State the blood parasite species.
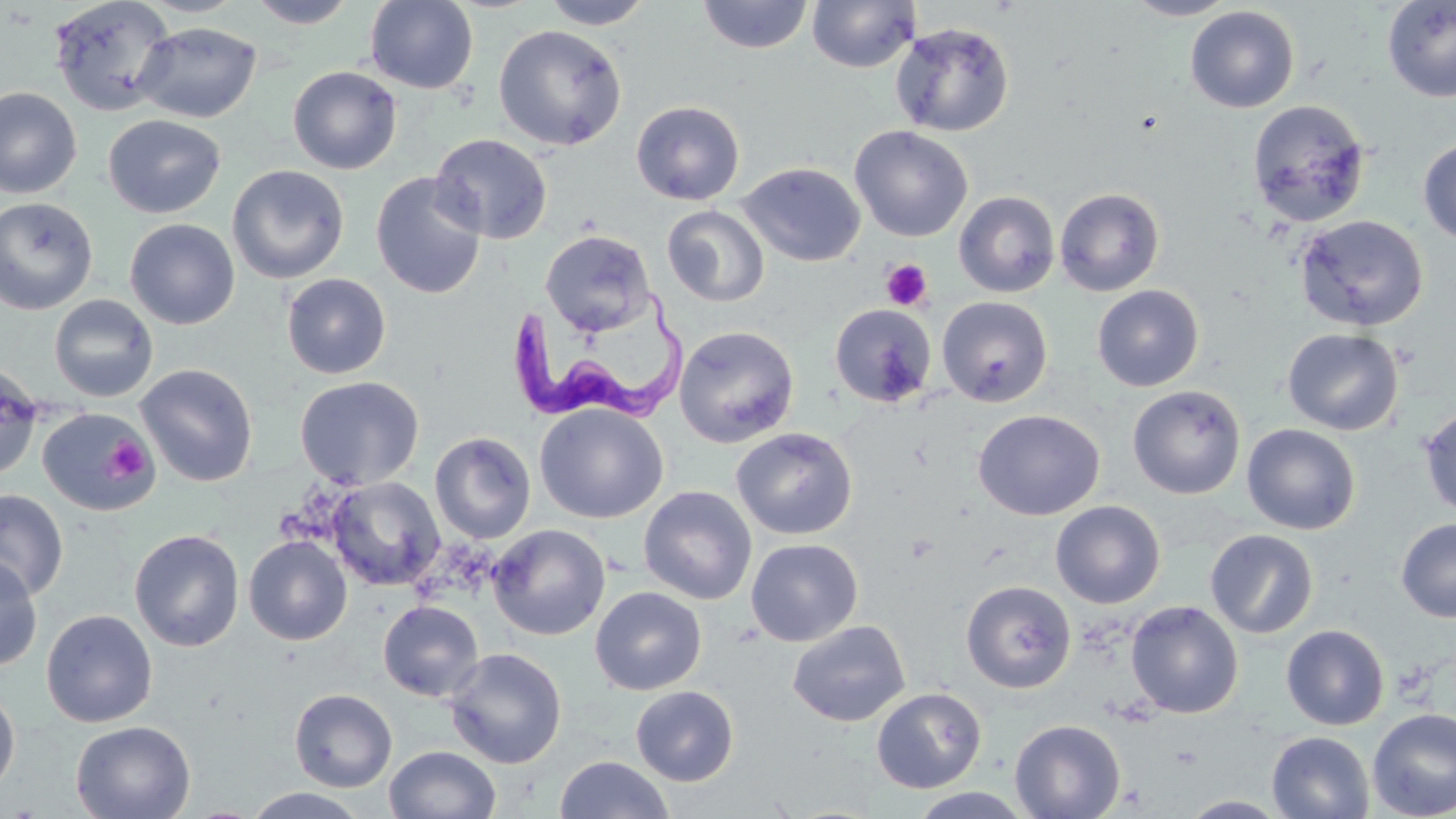
Trypanosoma brucei.

Summary:
  - Coordinate format: approximate bounding boxes as (x1, y1, x2, y2) in pixels
  - Platelet locations: (881, 259, 933, 311), (104, 437, 152, 482)
  - Trypanosoma brucei locations: (505, 288, 690, 426)
  - Uninfected red blood cell locations: (49, 0, 176, 117), (139, 0, 246, 17), (245, 0, 359, 29), (365, 0, 479, 94), (541, 0, 655, 29), (697, 0, 814, 54), (806, 0, 920, 73), (1123, 0, 1240, 20), (1382, 1, 1456, 103), (1185, 6, 1300, 113), (134, 21, 262, 123), (890, 22, 1015, 137), (493, 24, 628, 151), (287, 66, 402, 174), (0, 87, 82, 199), (1247, 99, 1371, 227), (631, 100, 745, 205), (102, 114, 226, 219), (849, 125, 973, 242), (430, 133, 552, 244), (1418, 138, 1456, 245), (737, 162, 865, 267), (227, 164, 349, 284), (370, 172, 487, 299), (1054, 187, 1165, 296), (954, 191, 1059, 297), (0, 196, 98, 315), (662, 206, 769, 306), (1295, 215, 1429, 332), (124, 218, 240, 329), (540, 229, 655, 336), (281, 273, 391, 379), (1092, 284, 1203, 391), (49, 295, 159, 402), (937, 297, 1052, 407), (829, 302, 938, 407), (674, 325, 799, 448), (1282, 328, 1403, 435), (0, 363, 44, 480), (135, 363, 258, 487), (294, 375, 425, 490), (1128, 385, 1246, 499), (534, 403, 668, 523), (37, 407, 157, 516), (1419, 407, 1456, 520), (973, 409, 1105, 521), (1242, 424, 1360, 535), (731, 427, 858, 541), (430, 431, 536, 544), (325, 476, 445, 591), (638, 486, 757, 605), (0, 489, 68, 601), (1051, 500, 1165, 608), (1396, 519, 1455, 622), (488, 524, 610, 640), (129, 529, 244, 651), (1205, 529, 1318, 639), (243, 536, 352, 645), (746, 538, 863, 646), (0, 555, 42, 672), (961, 580, 1076, 693), (590, 587, 707, 695), (378, 600, 484, 702), (1126, 600, 1244, 719), (41, 609, 158, 727), (788, 621, 911, 727), (1281, 624, 1389, 730), (444, 647, 567, 769), (0, 684, 21, 798), (631, 686, 739, 786), (289, 688, 397, 792), (871, 688, 987, 793), (1367, 708, 1456, 819), (1010, 719, 1125, 819), (70, 720, 196, 818), (1266, 731, 1375, 818), (384, 745, 501, 819), (554, 755, 674, 819), (243, 787, 370, 819), (908, 787, 1035, 818), (1176, 795, 1292, 817)
  - Modality: light microscopy
  - Field of view: one of a larger specimen
  - Preparation: thin blood smear
  - Image size: 1456×819 pixels
  - Magnification: 1000x
  - Stain: May-Grünwald-Giemsa